Assess for malaria.
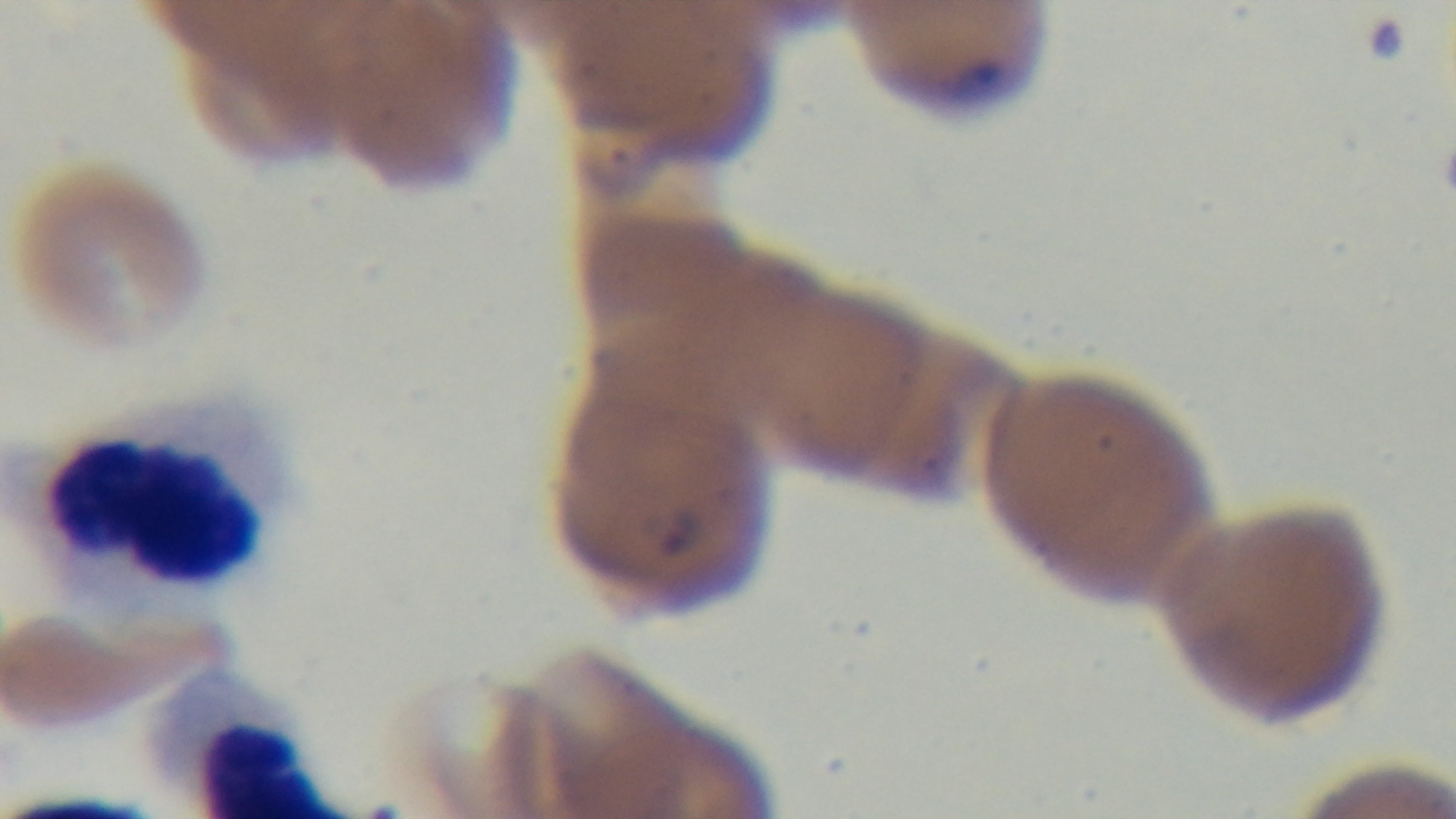
It is infected.

Summary:
  - Preparation: thin smear
  - Objective: 100x oil immersion
  - Field of view: one from the slide
  - Capture: mounted 4K digital camera
  - Stain: Giemsa
  - Modality: light microscopy